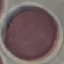
{
  "result": "no malaria parasites seen",
  "stain": "Giemsa",
  "capture": "smartphone through the microscope eyepiece",
  "preparation": "thin smear",
  "image_type": "automatically extracted cell patch, resized to 64 × 64 pixels"
}